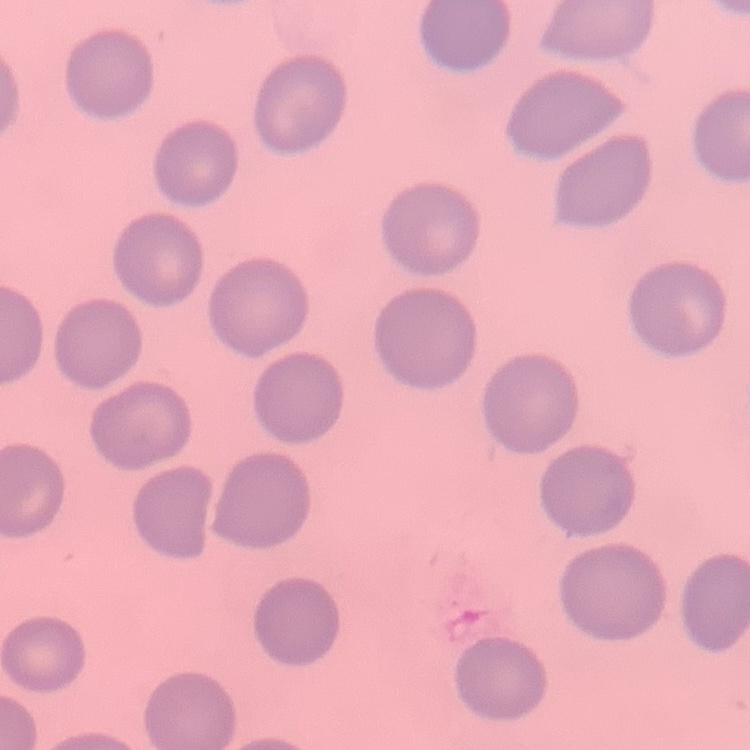

The erythrocytes exhibit no rouleaux formation. Thin blood film. Stained with either Field's or Giemsa. One tile cut from a larger photomicrograph.